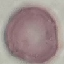

Malaria status: uninfected. Giemsa-stained preparation. Thin smear of blood. Automatically extracted cell patch, resized to 64 × 64 pixels. Photographed with a smartphone camera at the microscope eyepiece.